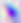

magnification = 400x
identification = Toxoplasma gondii
modality = photomicrograph